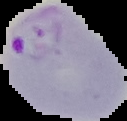

image size = 127×121 pixels
preparation = thin blood smear
result = malaria parasites identified
image type = cell region segmented out of the field of view; surrounding area masked to black